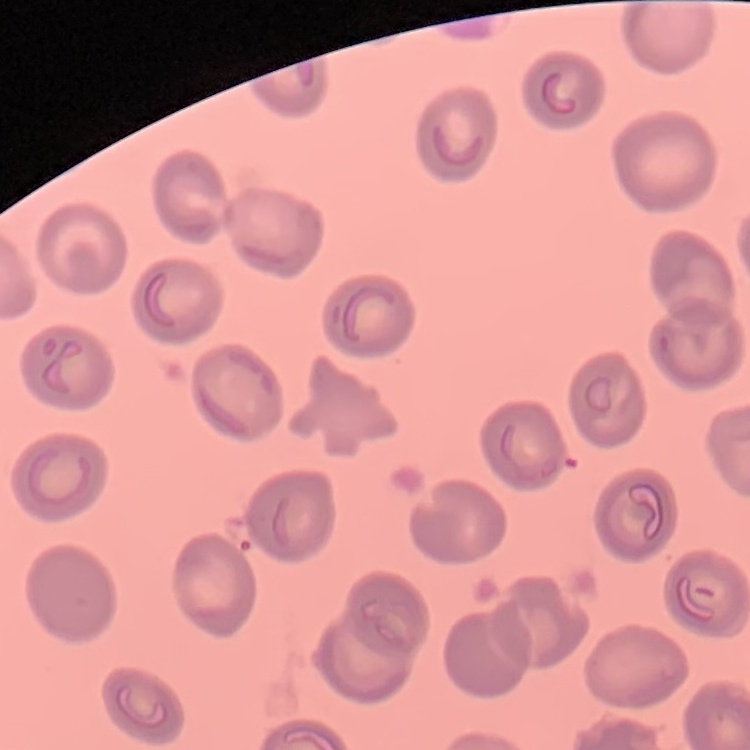

Summary:
  - Erythrocyte morphology: no rouleaux formation
  - Image type: one tile cut from a larger photomicrograph
  - Preparation: thin blood film
  - Stain: Field's or Giemsa